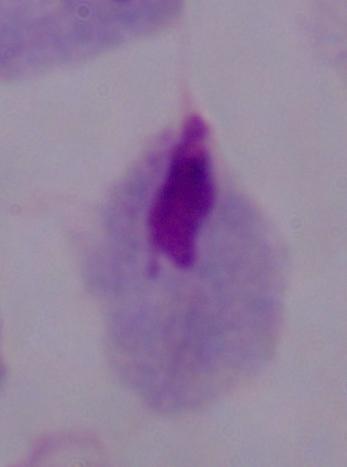
A trichomonad is shown. 1000x magnification. Photomicrograph.